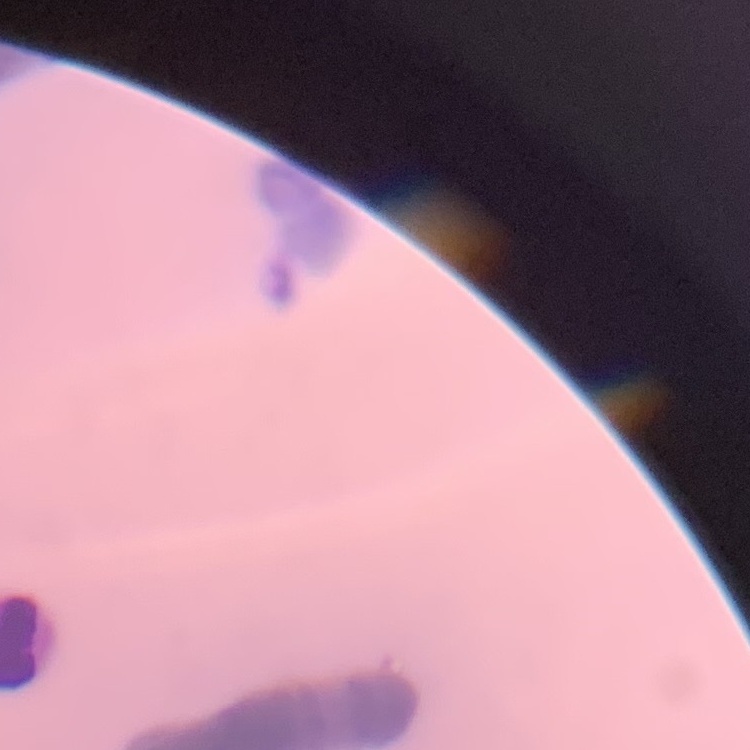
Summary:
  - Erythrocyte morphology: rouleaux formation
  - Stain: Field's or Giemsa
  - Preparation: thin blood smear
  - Image type: square crop of a larger photomicrograph